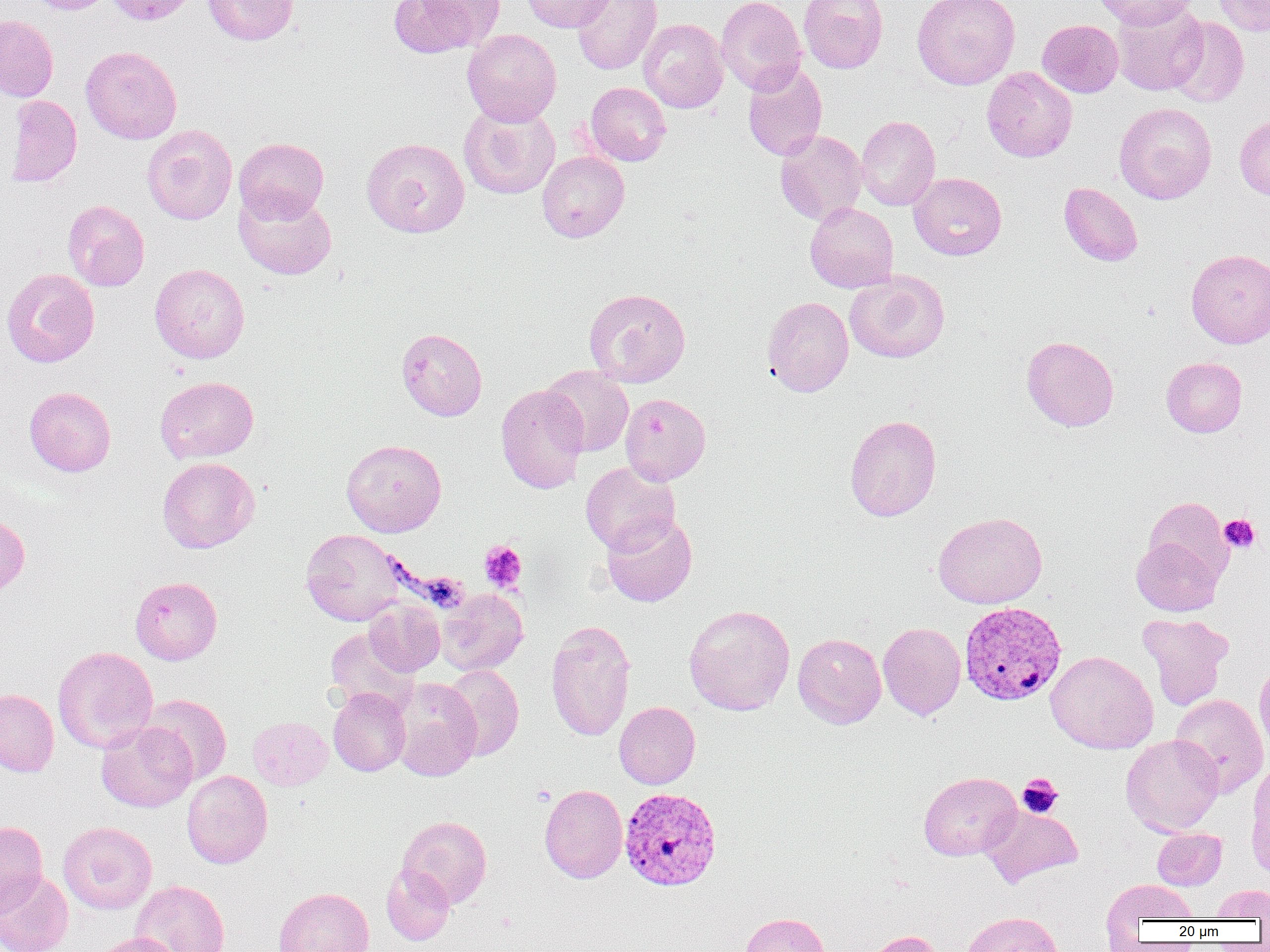
Summary:
  - Coordinate format: approximate bounding boxes as (x1, y1, x2, y2) in pixels
  - Uninfected red blood cell locations: (25, 0, 114, 14), (106, 0, 198, 26), (203, 0, 299, 45), (388, 0, 503, 58), (522, 0, 615, 32), (571, 0, 662, 75), (716, 0, 807, 94), (798, 0, 888, 73), (912, 0, 1020, 90), (1093, 0, 1199, 29), (1212, 0, 1270, 36), (1111, 2, 1208, 96), (0, 14, 58, 102), (1167, 16, 1249, 107), (638, 18, 729, 112), (1037, 19, 1123, 97), (462, 29, 561, 126), (81, 45, 182, 144), (742, 63, 828, 161), (981, 67, 1077, 162), (585, 82, 671, 166), (5, 94, 82, 187), (459, 102, 560, 199), (1114, 102, 1217, 204), (1235, 114, 1270, 201), (856, 115, 940, 211), (141, 124, 237, 224), (775, 129, 867, 225), (234, 137, 329, 223), (361, 137, 470, 238), (537, 151, 629, 242), (908, 172, 1007, 260), (1059, 182, 1143, 266), (234, 188, 337, 280), (62, 199, 150, 291), (805, 202, 898, 293), (1186, 249, 1270, 348), (150, 263, 250, 363), (2, 268, 99, 367), (845, 270, 949, 363), (583, 287, 691, 387), (762, 296, 853, 397), (396, 328, 487, 421), (1021, 336, 1119, 432), (1161, 357, 1247, 437), (541, 366, 634, 457), (155, 376, 259, 464), (496, 384, 589, 494), (24, 386, 116, 477), (620, 393, 711, 485), (844, 414, 942, 522), (341, 439, 446, 537), (157, 457, 260, 553), (580, 461, 680, 555), (1143, 497, 1232, 582), (0, 511, 30, 596), (933, 512, 1047, 609), (601, 513, 697, 607), (300, 529, 409, 626), (1131, 535, 1224, 616), (130, 576, 222, 664), (436, 588, 528, 675), (364, 599, 445, 676), (684, 604, 795, 716), (1137, 613, 1234, 710), (546, 618, 636, 742), (878, 622, 966, 720), (324, 628, 417, 714), (793, 633, 886, 728), (52, 646, 158, 753), (1045, 650, 1159, 754), (1254, 656, 1270, 757), (441, 665, 524, 761), (391, 678, 481, 781), (328, 688, 411, 776), (0, 689, 59, 777), (139, 694, 232, 785), (1170, 694, 1269, 797), (614, 701, 700, 789), (248, 716, 333, 790), (95, 720, 196, 812), (1121, 734, 1224, 836), (1247, 761, 1270, 876), (182, 770, 273, 868), (918, 771, 1021, 861), (539, 784, 627, 883), (980, 805, 1082, 888), (397, 816, 492, 908), (0, 820, 48, 915), (58, 821, 157, 914), (1152, 828, 1227, 890), (381, 864, 454, 945), (0, 869, 73, 952), (1102, 878, 1198, 929), (130, 880, 230, 952), (1212, 884, 1270, 920), (274, 887, 373, 952), (961, 911, 1063, 952), (739, 912, 830, 952), (865, 930, 944, 952), (90, 933, 183, 952)
  - Platelet locations: (1219, 514, 1260, 553), (479, 540, 527, 593), (1017, 774, 1062, 818)
  - Plasmodium vivax-infected red blood cell locations: (959, 601, 1068, 706), (619, 787, 722, 891)
  - Slide-level diagnosis: Plasmodium vivax
  - Preparation: thin blood film
  - Modality: optical microscopy
  - Image size: 1270×952 pixels
  - Field of view: single
  - Magnification: 1000x